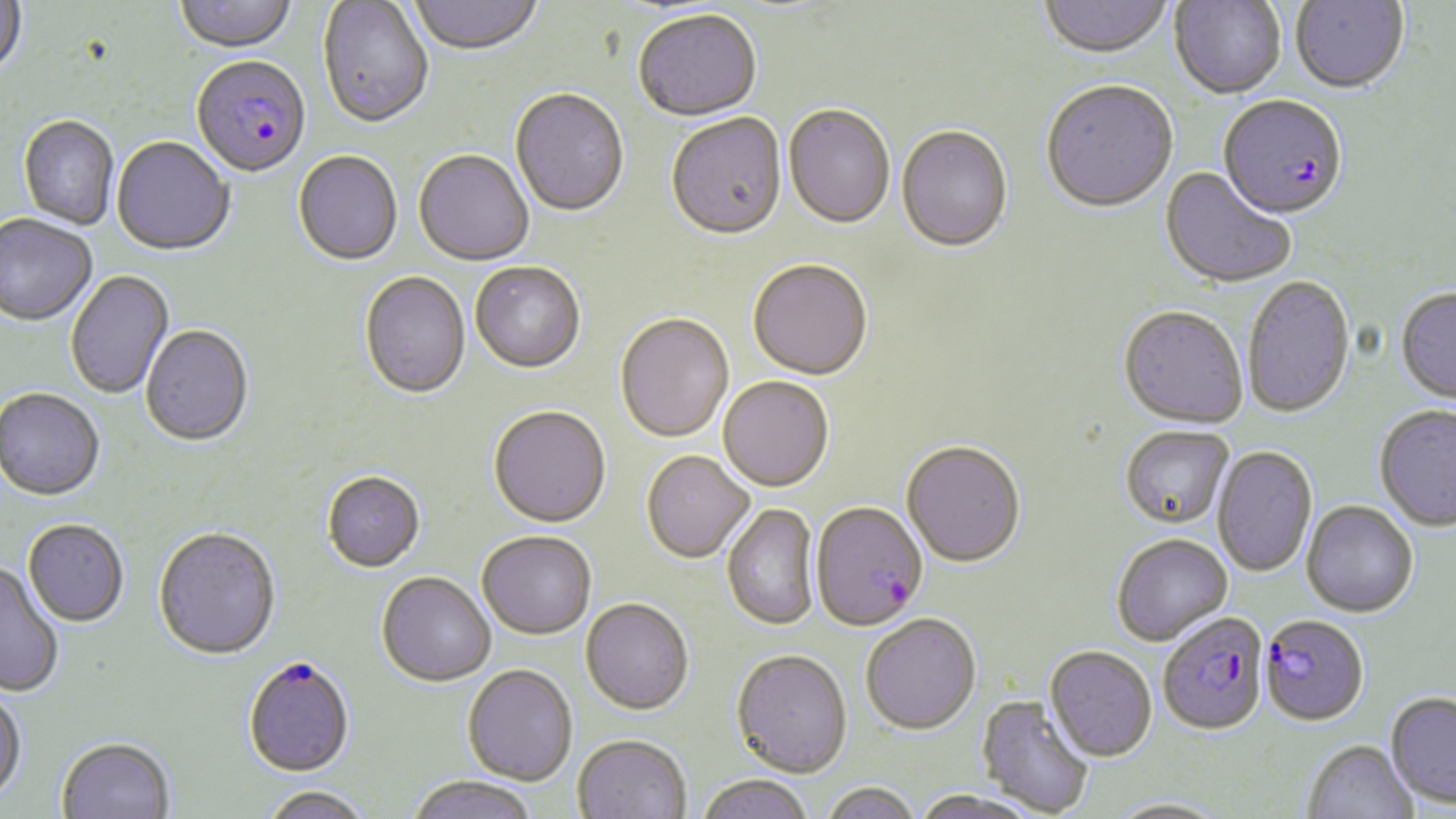

slide-level diagnosis = Plasmodium falciparum
stain = May-Grünwald-Giemsa
preparation = thin blood smear
image size = 1456×819 pixels
modality = light microscopy
field of view = one of a larger specimen
uninfected red blood cell locations = approximate bounding boxes as (x1, y1, x2, y2) in pixels: (0, 0, 27, 80), (173, 0, 298, 55), (408, 0, 544, 58), (1039, 0, 1173, 61), (1290, 0, 1409, 96), (317, 1, 434, 131), (1170, 1, 1286, 100), (632, 12, 762, 124), (1041, 83, 1179, 215), (510, 90, 629, 219), (783, 106, 895, 231), (665, 115, 788, 243), (18, 117, 119, 230), (896, 127, 1013, 255), (111, 138, 234, 258), (413, 152, 533, 268), (293, 153, 403, 267), (1159, 168, 1296, 290), (0, 216, 97, 328), (748, 261, 872, 382), (470, 263, 585, 375), (66, 270, 174, 399), (359, 273, 471, 401), (1243, 276, 1356, 419), (1395, 287, 1456, 405), (1118, 307, 1248, 430), (615, 314, 734, 444), (141, 326, 254, 448), (718, 377, 834, 492), (0, 390, 104, 502), (1374, 404, 1456, 531), (488, 407, 611, 529), (1121, 425, 1233, 528), (901, 441, 1027, 568), (1213, 445, 1317, 578), (641, 451, 754, 563), (322, 472, 425, 573), (1302, 500, 1418, 617), (722, 503, 820, 631), (22, 521, 129, 628), (152, 528, 280, 661), (477, 531, 596, 640), (1111, 533, 1233, 645), (0, 563, 64, 698), (376, 573, 495, 688), (581, 599, 694, 716), (861, 613, 982, 736), (1045, 645, 1157, 761), (731, 649, 852, 778), (462, 665, 577, 786), (0, 687, 27, 804), (1386, 691, 1456, 808), (977, 695, 1095, 817), (573, 735, 692, 819), (56, 738, 175, 819), (1302, 739, 1418, 819), (695, 774, 814, 819), (406, 776, 539, 819), (820, 781, 921, 819), (260, 786, 374, 819), (910, 788, 1046, 819), (1108, 798, 1229, 818)
magnification = 1000x
Plasmodium falciparum-infected red blood cell locations = approximate bounding boxes as (x1, y1, x2, y2) in pixels: (191, 57, 311, 181), (1218, 98, 1348, 223), (810, 501, 928, 631), (1157, 611, 1269, 734), (1259, 614, 1370, 726), (243, 657, 355, 778)